Report the malaria status of this cell.
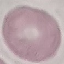

It is uninfected.

Thin smear of blood. Photographed with a smartphone camera at the microscope eyepiece. Cell patch, automatically extracted from a larger field of view and resized to 64 × 64 pixels. Giemsa stain.